Identify the cell.
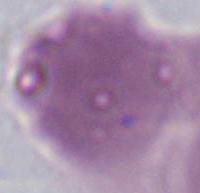

This is an erythrocyte.

Summary:
  - Magnification: 1000x
  - Modality: micrograph